Classify this cell by malaria status.
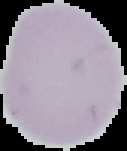

It is uninfected.

Summary:
  - Image type: segmented cell region with the area outside set to black
  - Image size: 127×151 pixels
  - Preparation: thin blood smear